Report the malaria status of this cell.
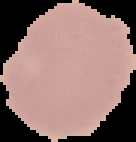

Uninfected.

Summary:
  - Image size: 136×142 pixels
  - Image type: cell region segmented out of the field of view; surrounding area masked to black
  - Preparation: thin blood film